Assess this cell for malaria.
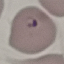
It is parasitized.

Summary:
  - Preparation: thin blood smear
  - Capture: smartphone camera at the microscope eyepiece
  - Stain: Giemsa
  - Image type: automatically extracted cell patch, resized to 64 × 64 pixels